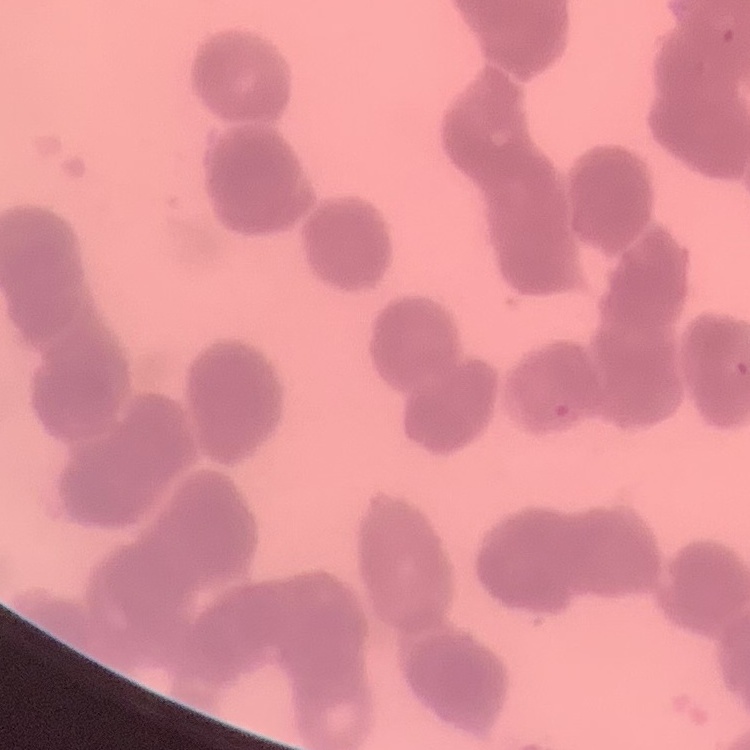
red blood cell morphology = rouleaux formation
stain = Field's or Giemsa
image type = one tile cut from a larger photomicrograph
preparation = thin peripheral smear